Give the position of every malaria parasite.
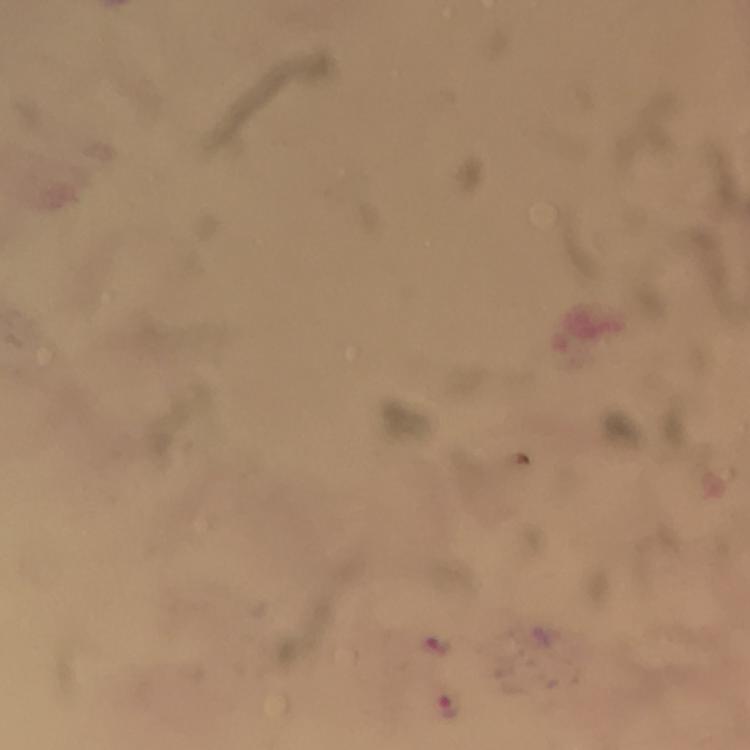

Approximate centers as (x, y) in pixels.
Malaria parasites: (437, 644), (448, 707).

Cropped region of a single field of view. Photographed with a smartphone mounted on the microscope. From a malaria diagnostic workup. Giemsa-stained preparation. Thick blood smear. Immersion oil applied. At 100x magnification. Image is 750×750 pixels.